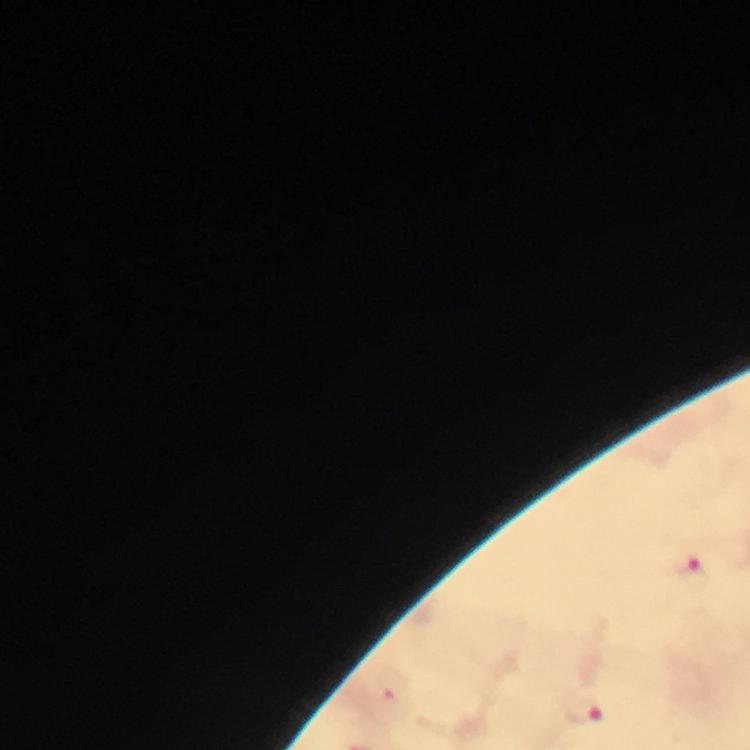
Approximate centers as (x, y) in pixels.
Summary:
  - Plasmodium parasite locations: (692, 572), (395, 687), (585, 713)
  - Preparation: thick blood smear
  - Context: from a diagnostic examination for malaria
  - Capture: smartphone mounted on the microscope
  - Cropped from: one field of view
  - Stain: Giemsa
  - Magnification: 100x
  - Immersion oil: applied
  - Image size: 750×750 pixels